Report the malaria status of this cell.
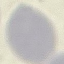
Uninfected.

stain: Giemsa
capture: smartphone through the microscope eyepiece
preparation: thin blood film
image_type: automatically extracted cell patch, resized to 64 × 64 pixels